Locate every blood parasite and identify its species.
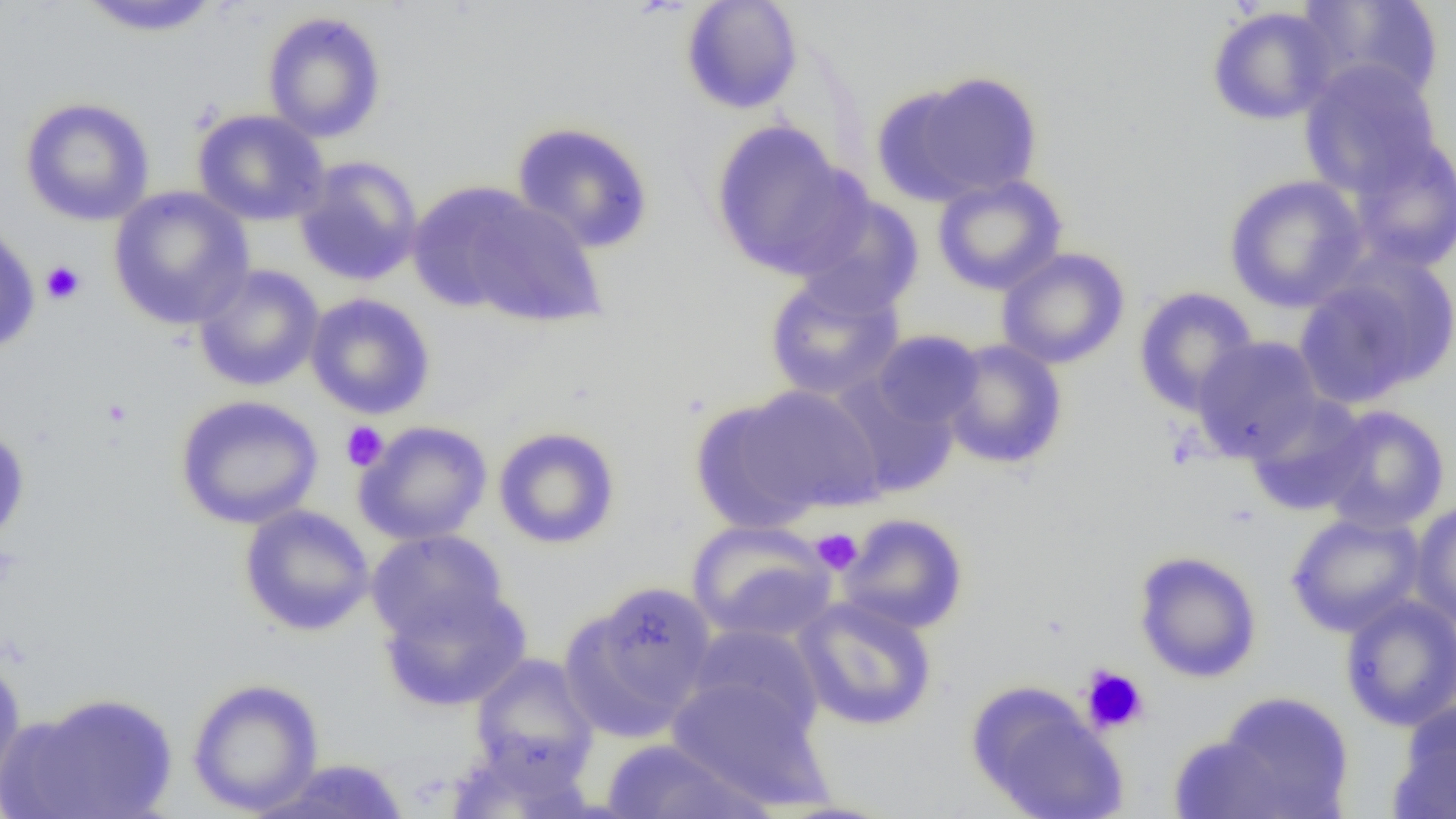

No blood parasites observed.

Summary:
  - Coordinate format: approximate bounding boxes as (x1,y1)-(x2,y2) corner pairs in pixels
  - Uninfected red blood cell locations: (680,0)-(803,115), (1294,0)-(1445,106), (75,1)-(224,37), (1206,6)-(1339,126), (262,11)-(386,143), (1298,60)-(1444,198), (882,70)-(1044,205), (19,97)-(155,227), (192,108)-(329,227), (510,120)-(654,254), (709,120)-(862,279), (1344,134)-(1455,274), (293,155)-(423,287), (932,174)-(1068,295), (1223,175)-(1369,313), (428,185)-(607,328), (108,186)-(255,330), (792,191)-(925,317), (0,220)-(40,355), (995,247)-(1130,369), (1294,259)-(1455,409), (192,264)-(325,392), (764,274)-(905,402), (1133,286)-(1260,416), (305,293)-(436,419), (870,330)-(985,430), (1190,335)-(1325,461), (941,339)-(1067,469), (827,374)-(961,498), (720,384)-(886,518), (1243,394)-(1373,516), (173,395)-(324,529), (1316,404)-(1450,533), (354,420)-(493,546), (0,425)-(31,550), (493,426)-(621,549), (1409,500)-(1456,630), (239,504)-(375,636), (1285,511)-(1425,637), (837,513)-(969,634), (687,519)-(838,643), (366,529)-(509,645), (1133,550)-(1263,683), (567,581)-(717,738), (378,584)-(532,712), (1339,593)-(1456,731), (792,596)-(938,732), (686,623)-(824,741), (0,653)-(27,796), (468,653)-(599,781), (667,676)-(830,809), (187,677)-(324,815), (966,681)-(1127,819), (6,691)-(178,819), (1207,692)-(1355,816), (1391,701)-(1456,818), (450,733)-(593,819), (1167,733)-(1297,819), (599,739)-(770,819), (253,758)-(413,818)
  - Platelet locations: (40,260)-(86,305), (101,398)-(133,428), (341,421)-(389,472), (811,528)-(863,574), (1080,665)-(1149,735)
  - Slide-level diagnosis: no evidence of blood parasites
  - Field of view: one of a larger specimen
  - Preparation: thin blood film
  - Modality: light microscopy
  - Magnification: 1000x
  - Image size: 1456×819 pixels